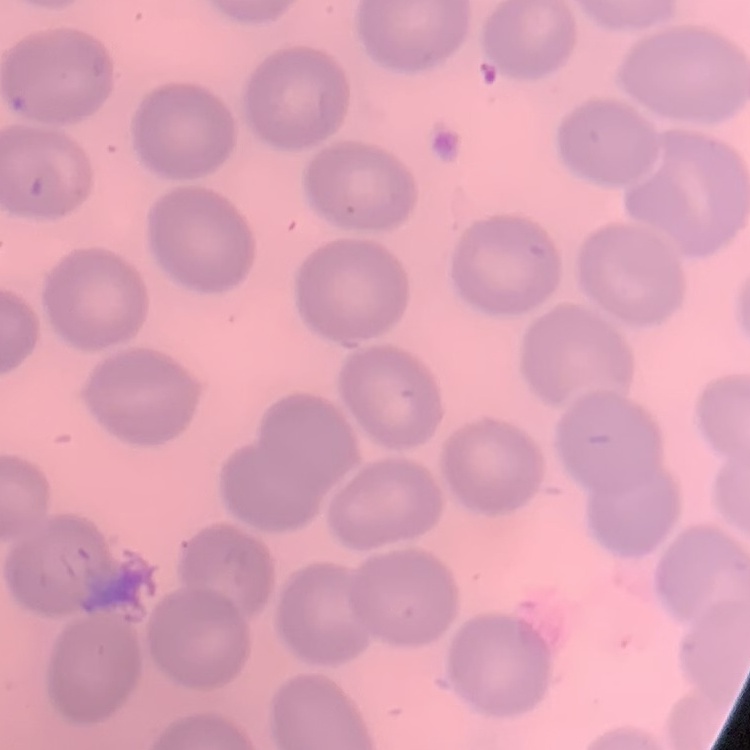

The erythrocytes exhibit no rouleaux formation. One tile cut from a larger photomicrograph. Stained with either Field's or Giemsa. Thin blood film.